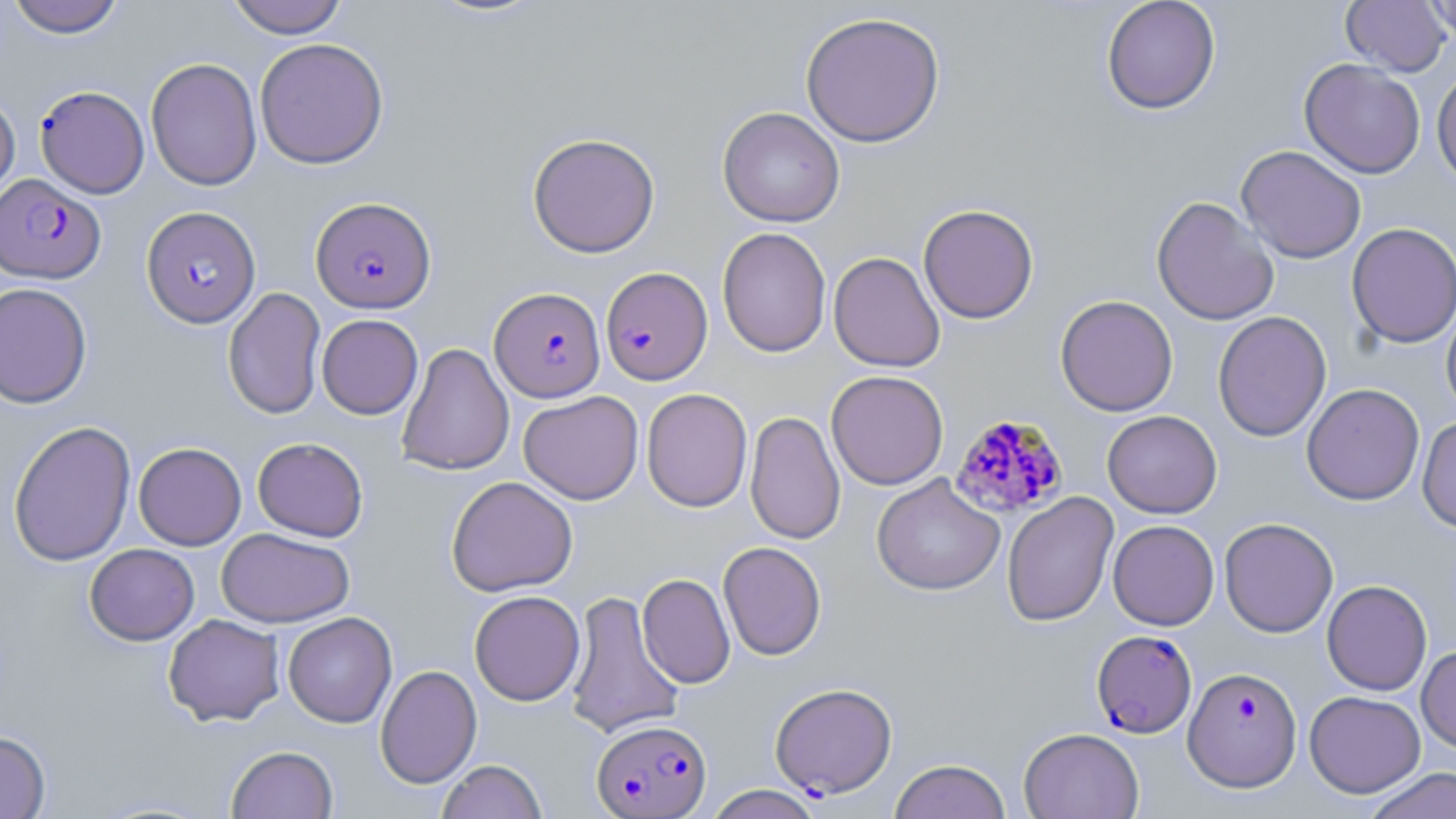
{
  "slide_level_diagnosis": "Plasmodium falciparum",
  "magnification": "1000x",
  "stain": "May-Grünwald-Giemsa",
  "modality": "light microscopy",
  "plasmodium_falciparum_infected_red_blood_cell_locations": "approximate bounding boxes as [x1, y1, x2, y2] in pixels: [36, 85, 149, 199], [0, 173, 106, 284], [311, 197, 436, 313], [141, 206, 261, 327], [600, 266, 713, 385], [490, 286, 606, 401], [949, 413, 1068, 519], [1091, 630, 1197, 739], [1183, 666, 1302, 791], [770, 682, 897, 799], [592, 718, 711, 818]",
  "image_size": "1456×819 pixels",
  "uninfected_red_blood_cell_locations": "approximate bounding boxes as [x1, y1, x2, y2] in pixels: [7, 0, 125, 38], [225, 0, 349, 38], [1100, 0, 1221, 114], [1340, 0, 1452, 76], [1424, 0, 1456, 46], [800, 11, 946, 148], [254, 37, 389, 169], [145, 57, 262, 191], [1299, 58, 1426, 179], [1432, 67, 1456, 188], [0, 91, 20, 206], [717, 106, 845, 227], [527, 132, 660, 258], [1236, 145, 1366, 264], [1151, 195, 1279, 326], [918, 204, 1039, 324], [1346, 222, 1456, 348], [717, 227, 831, 357], [828, 251, 945, 372], [0, 282, 93, 409], [222, 287, 326, 420], [1055, 295, 1179, 416], [1441, 301, 1456, 419], [1212, 311, 1331, 442], [316, 314, 423, 419], [396, 342, 514, 476], [825, 370, 949, 490], [1301, 384, 1425, 506], [641, 388, 753, 512], [518, 390, 643, 505], [744, 410, 845, 545], [1102, 410, 1222, 518], [1417, 416, 1456, 533], [8, 420, 136, 567], [252, 437, 369, 541], [134, 442, 246, 550], [871, 473, 1005, 596], [446, 475, 578, 597], [1002, 492, 1118, 627], [1219, 517, 1338, 637], [1108, 520, 1220, 630], [217, 527, 355, 627], [718, 541, 827, 661], [84, 543, 199, 645], [637, 573, 735, 689], [1322, 579, 1432, 696], [469, 590, 585, 706], [564, 590, 685, 739], [283, 612, 397, 728], [163, 613, 285, 726], [1416, 644, 1456, 754], [375, 664, 482, 789], [1304, 690, 1426, 798], [1018, 727, 1144, 819], [0, 729, 50, 818], [226, 745, 338, 818], [889, 758, 1012, 819], [437, 760, 547, 819], [1362, 766, 1456, 819], [705, 784, 824, 819]",
  "field_of_view": "single",
  "preparation": "thin blood smear"
}